Give the extent of all uninfected red blood cells.
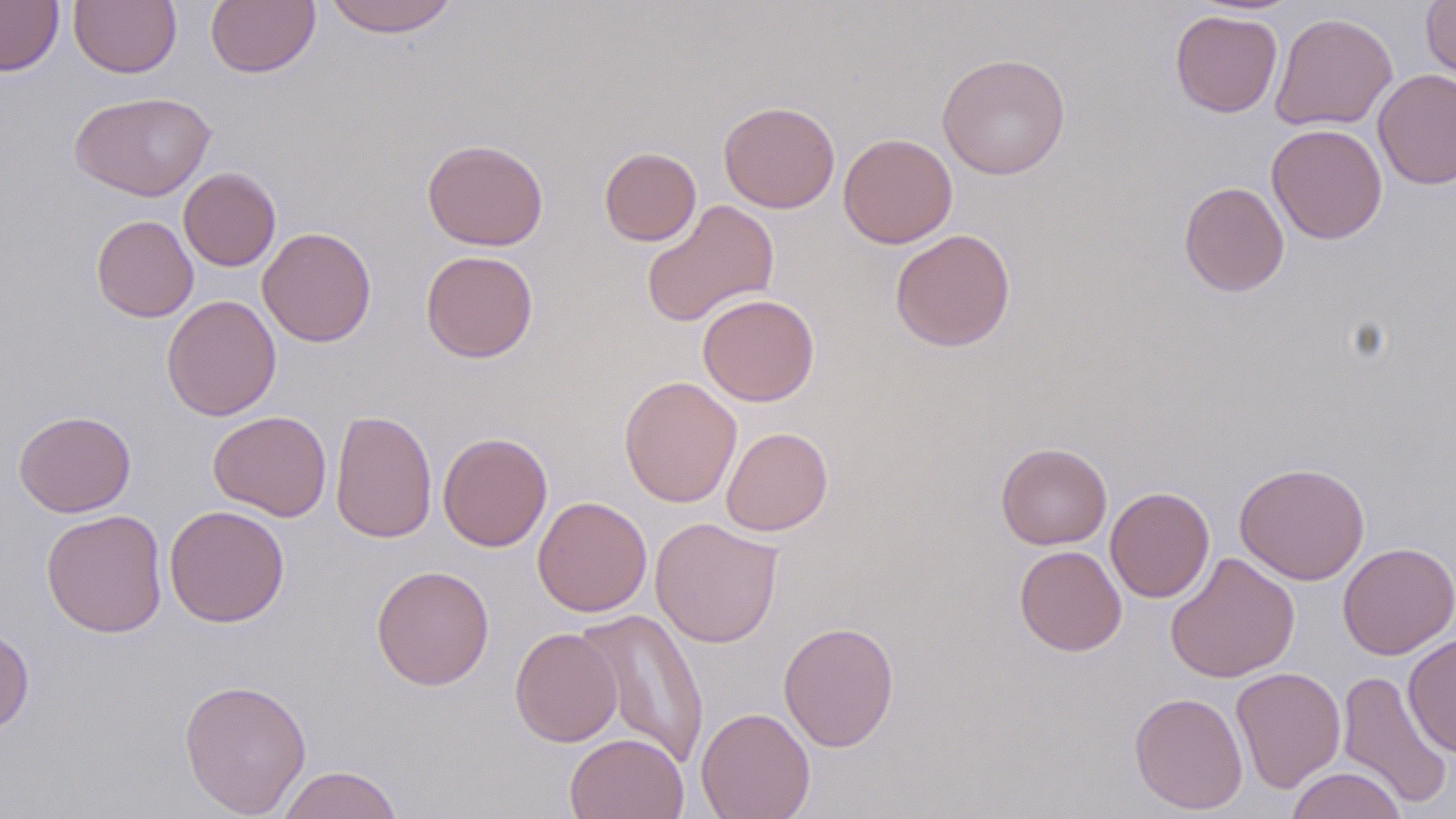

Approximate bounding boxes as (x1,y1)-(x2,y2) corner pairs in pixels.
Uninfected red blood cells: (0,0)-(64,76), (206,0)-(320,78), (324,0)-(458,37), (69,1)-(181,77), (1420,1)-(1456,83), (1170,10)-(1283,118), (1269,12)-(1398,132), (936,52)-(1071,180), (1373,69)-(1456,189), (69,91)-(216,202), (718,101)-(840,213), (1266,124)-(1387,243), (838,133)-(958,248), (422,139)-(549,251), (599,146)-(701,246), (178,167)-(281,271), (1179,181)-(1289,297), (641,199)-(779,328), (91,214)-(198,322), (257,226)-(377,347), (889,229)-(1016,352), (420,249)-(538,363), (697,293)-(820,407), (161,294)-(282,421), (619,375)-(742,507), (330,408)-(438,544), (14,410)-(136,517), (208,411)-(332,521), (721,426)-(833,535), (438,431)-(553,552), (996,442)-(1112,549), (1234,462)-(1370,585), (1105,486)-(1214,603), (532,496)-(652,616), (164,504)-(289,627), (41,509)-(168,638), (649,517)-(783,648), (1337,542)-(1456,660), (1014,545)-(1127,656), (1165,551)-(1301,683), (371,565)-(495,690), (576,608)-(710,768), (778,621)-(899,751), (0,623)-(35,738), (509,627)-(622,747), (1403,632)-(1456,758), (1230,667)-(1346,792), (1337,669)-(1453,809), (178,678)-(312,818), (1130,692)-(1249,814), (696,707)-(815,819), (565,732)-(688,819), (277,765)-(403,819), (1285,766)-(1408,819).

Summary:
  - Slide-level diagnosis: no evidence of blood parasites
  - Image size: 1456×819 pixels
  - Field of view: single
  - Stain: May-Grünwald-Giemsa
  - Preparation: thin blood film
  - Magnification: 1000x
  - Modality: optical microscopy